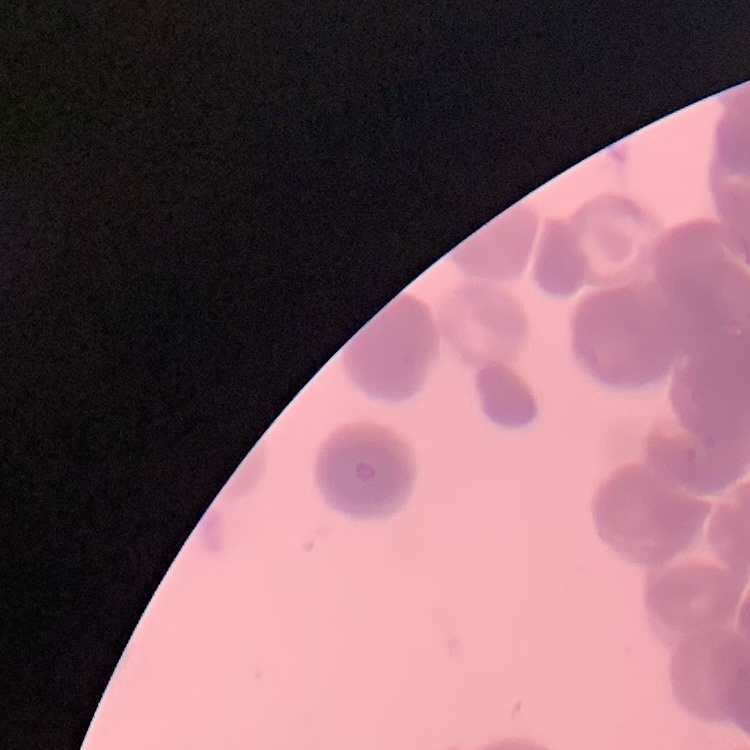
Summary:
  - Erythrocyte morphology: rouleaux formation
  - Image type: one tile cut from a larger photomicrograph
  - Preparation: thin blood smear
  - Stain: Field's or Giemsa